State the blood parasite species.
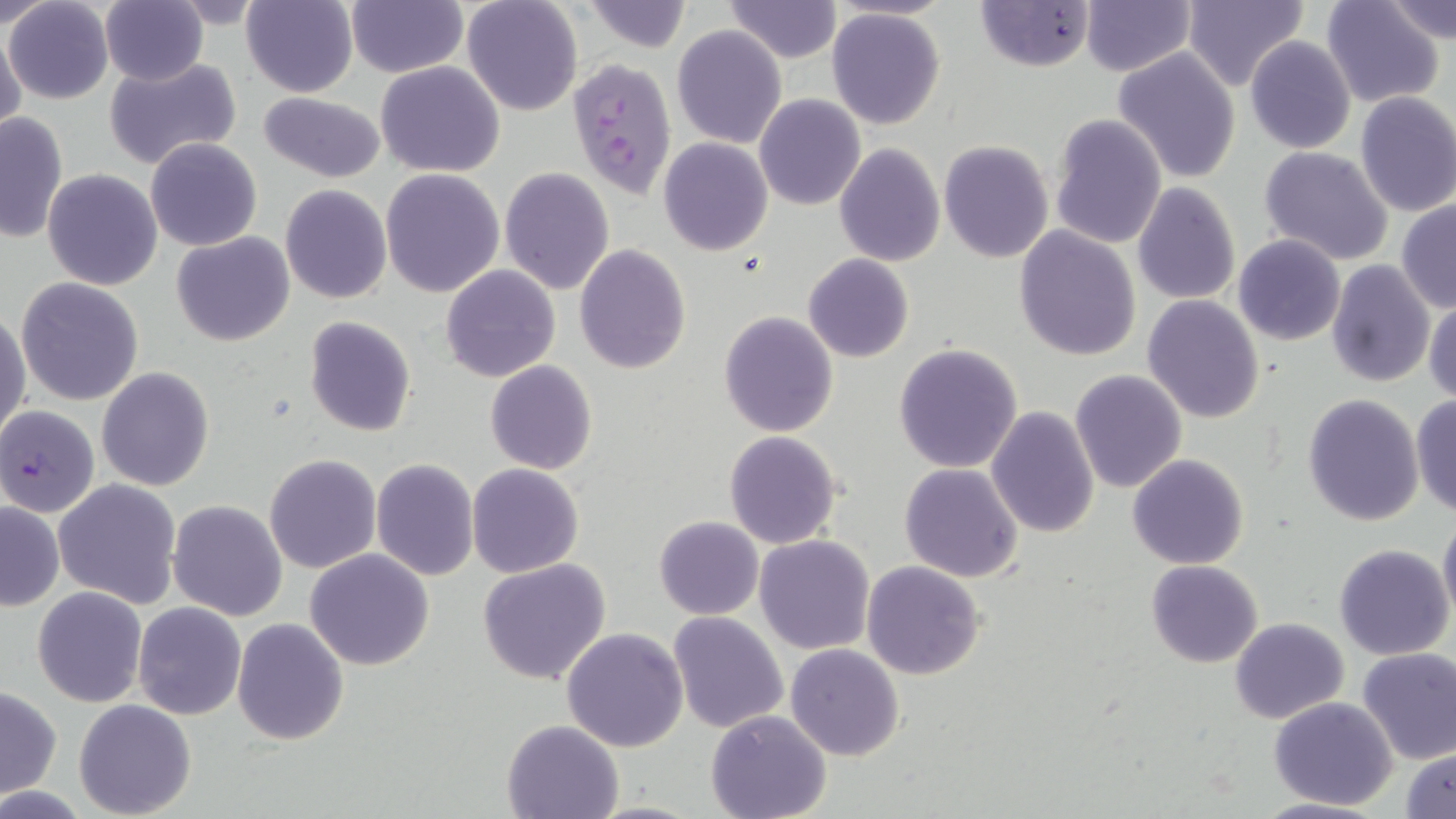

Plasmodium falciparum.

Summary:
  - Coordinate format: approximate bounding boxes as named x1/y1/x2/y2 corners in pixels
  - Plasmodium falciparum-infected red blood cell locations: (x1=568, y1=58, x2=678, y2=198), (x1=1, y1=404, x2=100, y2=518)
  - Uninfected red blood cell locations: (x1=0, y1=0, x2=57, y2=27), (x1=5, y1=0, x2=113, y2=104), (x1=100, y1=0, x2=209, y2=86), (x1=242, y1=0, x2=359, y2=98), (x1=461, y1=0, x2=584, y2=117), (x1=581, y1=0, x2=692, y2=52), (x1=724, y1=0, x2=840, y2=63), (x1=1185, y1=0, x2=1309, y2=93), (x1=1385, y1=0, x2=1456, y2=46), (x1=974, y1=1, x2=1096, y2=73), (x1=1321, y1=1, x2=1446, y2=109), (x1=347, y1=2, x2=466, y2=77), (x1=1081, y1=2, x2=1195, y2=76), (x1=827, y1=8, x2=947, y2=129), (x1=1, y1=20, x2=25, y2=140), (x1=672, y1=24, x2=786, y2=147), (x1=1245, y1=35, x2=1356, y2=154), (x1=1112, y1=47, x2=1242, y2=182), (x1=104, y1=57, x2=242, y2=170), (x1=376, y1=61, x2=506, y2=178), (x1=258, y1=91, x2=386, y2=183), (x1=1354, y1=91, x2=1456, y2=217), (x1=754, y1=94, x2=866, y2=210), (x1=0, y1=111, x2=69, y2=243), (x1=1048, y1=112, x2=1166, y2=252), (x1=145, y1=137, x2=262, y2=251), (x1=658, y1=137, x2=773, y2=255), (x1=938, y1=139, x2=1054, y2=263), (x1=834, y1=142, x2=944, y2=267), (x1=1259, y1=145, x2=1395, y2=267), (x1=498, y1=167, x2=616, y2=296), (x1=43, y1=169, x2=163, y2=292), (x1=380, y1=169, x2=505, y2=298), (x1=1132, y1=182, x2=1241, y2=304), (x1=280, y1=185, x2=392, y2=303), (x1=1396, y1=199, x2=1455, y2=313), (x1=1015, y1=225, x2=1142, y2=360), (x1=172, y1=231, x2=294, y2=347), (x1=1233, y1=234, x2=1345, y2=346), (x1=573, y1=244, x2=691, y2=374), (x1=802, y1=253, x2=915, y2=362), (x1=1325, y1=259, x2=1436, y2=388), (x1=441, y1=265, x2=562, y2=382), (x1=15, y1=277, x2=145, y2=407), (x1=1142, y1=295, x2=1266, y2=423), (x1=1425, y1=295, x2=1456, y2=404), (x1=0, y1=309, x2=30, y2=447), (x1=717, y1=310, x2=840, y2=437), (x1=304, y1=316, x2=416, y2=437), (x1=893, y1=343, x2=1023, y2=472), (x1=485, y1=360, x2=598, y2=475), (x1=96, y1=367, x2=215, y2=492), (x1=1069, y1=368, x2=1188, y2=494), (x1=1302, y1=393, x2=1424, y2=526), (x1=1410, y1=395, x2=1456, y2=518), (x1=986, y1=405, x2=1100, y2=539), (x1=724, y1=430, x2=844, y2=549), (x1=264, y1=454, x2=380, y2=574), (x1=1127, y1=454, x2=1250, y2=569), (x1=370, y1=458, x2=480, y2=582), (x1=898, y1=462, x2=1023, y2=583), (x1=467, y1=463, x2=584, y2=577), (x1=53, y1=478, x2=182, y2=608), (x1=0, y1=500, x2=63, y2=611), (x1=168, y1=500, x2=289, y2=622), (x1=1438, y1=514, x2=1456, y2=628), (x1=653, y1=516, x2=763, y2=620), (x1=754, y1=535, x2=875, y2=656), (x1=1333, y1=543, x2=1453, y2=661), (x1=304, y1=549, x2=435, y2=671), (x1=478, y1=558, x2=612, y2=686), (x1=862, y1=560, x2=986, y2=680), (x1=1146, y1=560, x2=1263, y2=668), (x1=32, y1=586, x2=148, y2=708), (x1=133, y1=602, x2=248, y2=720), (x1=667, y1=612, x2=789, y2=733), (x1=1229, y1=617, x2=1348, y2=723), (x1=231, y1=619, x2=349, y2=745), (x1=561, y1=627, x2=689, y2=752), (x1=786, y1=644, x2=905, y2=762), (x1=1356, y1=648, x2=1456, y2=766), (x1=0, y1=687, x2=62, y2=797), (x1=1267, y1=696, x2=1398, y2=809), (x1=74, y1=700, x2=198, y2=818), (x1=705, y1=710, x2=833, y2=819), (x1=501, y1=718, x2=625, y2=818), (x1=1402, y1=747, x2=1456, y2=818), (x1=1250, y1=797, x2=1392, y2=819)
  - Stain: May-Grünwald-Giemsa
  - Preparation: thin blood film
  - Magnification: 1000x
  - Image size: 1456×819 pixels
  - Field of view: one of a larger specimen
  - Modality: light microscopy